Classify this cell by malaria status.
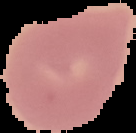
It is uninfected.

image type = cell region segmented out of the field of view; surrounding area masked to black
image size = 136×133 pixels
preparation = thin blood smear